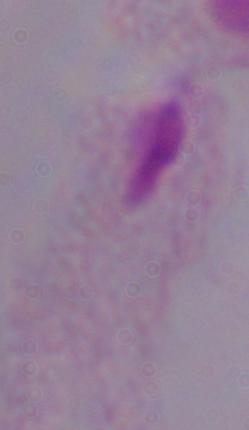
modality = micrograph
identification = trichomonad
magnification = 1000x